Identify the parasite.
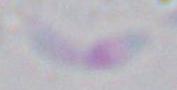

Toxoplasma gondii.

Micrograph. Captured at 1000x magnification.